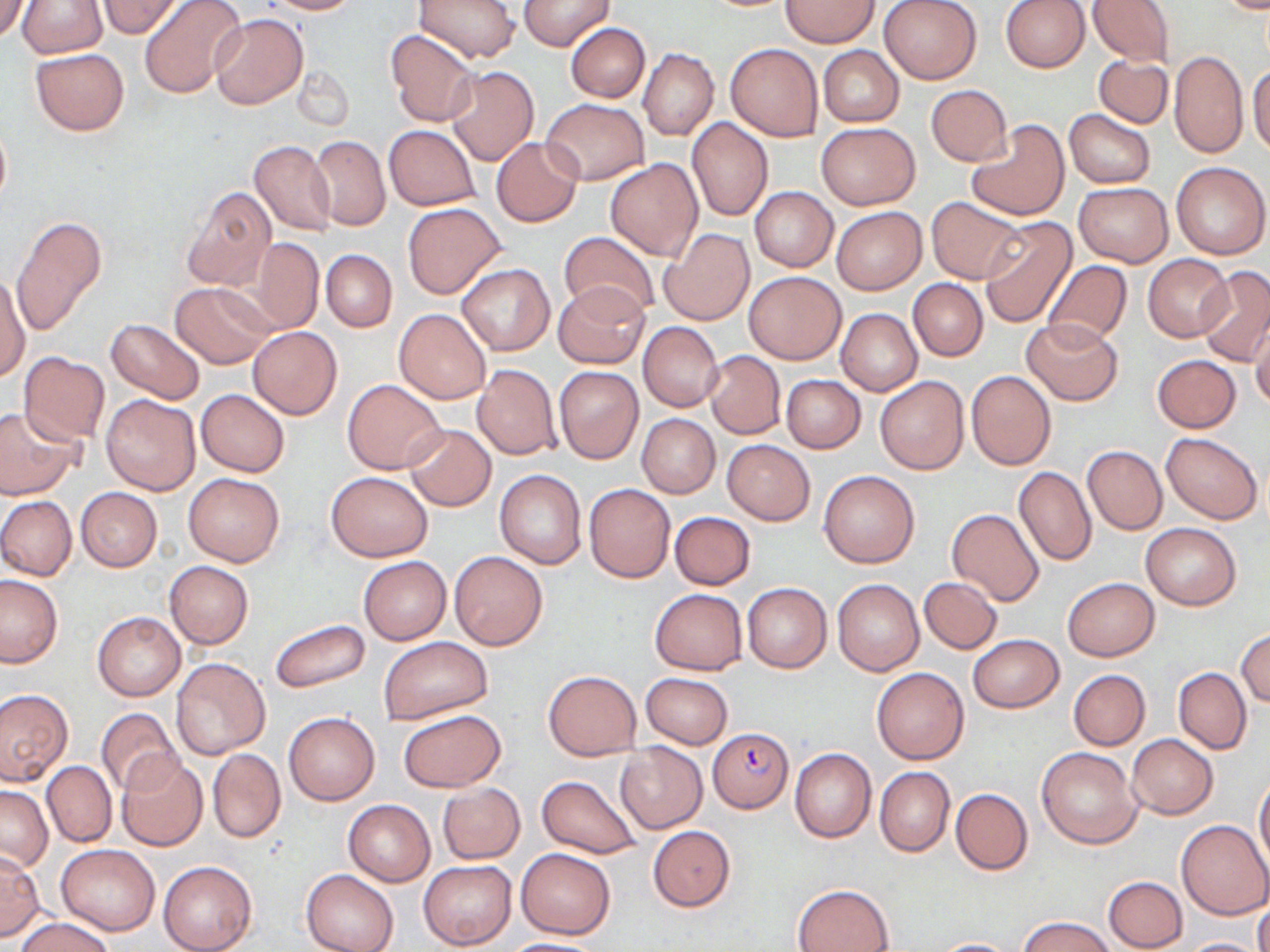
slide-level diagnosis = Plasmodium falciparum
uninfected red blood cell locations = approximate bounding boxes as [x1, y1, x2, y2] in pixels: [1, 0, 30, 41], [137, 0, 247, 99], [261, 0, 361, 15], [415, 0, 520, 64], [518, 0, 615, 51], [782, 0, 881, 47], [877, 0, 982, 84], [1000, 0, 1090, 72], [1087, 0, 1175, 66], [17, 1, 107, 58], [99, 1, 181, 37], [210, 13, 308, 110], [565, 22, 649, 102], [385, 29, 479, 127], [725, 43, 822, 141], [817, 45, 904, 127], [30, 48, 129, 136], [638, 49, 718, 140], [1169, 49, 1249, 159], [1092, 54, 1173, 129], [1248, 63, 1270, 157], [293, 66, 354, 131], [446, 66, 539, 166], [926, 85, 1013, 166], [540, 99, 650, 184], [1064, 109, 1155, 188], [0, 118, 11, 209], [687, 118, 774, 221], [816, 121, 919, 210], [966, 121, 1068, 221], [384, 125, 479, 210], [309, 135, 390, 231], [491, 137, 582, 227], [248, 139, 336, 237], [211, 146, 328, 292], [606, 158, 703, 261], [1170, 162, 1269, 259], [1075, 182, 1172, 265], [181, 186, 275, 292], [750, 186, 838, 272], [927, 196, 1028, 285], [402, 204, 506, 298], [832, 206, 927, 294], [10, 214, 106, 339], [977, 216, 1076, 328], [660, 229, 754, 325], [558, 231, 661, 321], [249, 239, 323, 331], [321, 249, 396, 332], [1144, 254, 1233, 341], [1042, 259, 1133, 347], [456, 264, 554, 356], [1196, 267, 1270, 367], [745, 272, 844, 364], [0, 275, 29, 382], [909, 280, 988, 360], [170, 283, 275, 370], [552, 283, 651, 369], [394, 308, 492, 404], [835, 308, 922, 397], [1249, 317, 1270, 411], [107, 318, 205, 405], [1021, 319, 1123, 405], [638, 322, 722, 412], [248, 326, 342, 419], [703, 350, 786, 439], [20, 353, 109, 443], [1152, 355, 1241, 432], [472, 365, 561, 459], [554, 366, 644, 463], [965, 370, 1057, 471], [782, 375, 865, 452], [875, 375, 969, 474], [343, 379, 446, 474], [196, 390, 289, 477], [102, 394, 201, 497], [0, 406, 80, 498], [637, 413, 721, 498], [404, 424, 496, 510], [1162, 432, 1262, 524], [721, 439, 815, 525], [1082, 446, 1167, 534], [1013, 466, 1096, 566], [818, 469, 919, 568], [495, 470, 587, 569], [183, 471, 284, 566], [326, 471, 433, 561], [584, 483, 675, 582], [77, 487, 162, 571], [0, 496, 76, 581], [946, 508, 1044, 608], [669, 512, 755, 589], [1140, 523, 1243, 609], [449, 552, 548, 650], [358, 555, 452, 644], [164, 560, 253, 649], [0, 575, 62, 667], [919, 576, 1001, 654], [1063, 577, 1158, 660], [832, 579, 924, 676], [741, 583, 832, 673], [649, 588, 747, 675], [93, 612, 185, 700], [270, 618, 371, 693], [1236, 628, 1270, 708], [967, 634, 1063, 712], [380, 637, 493, 722], [170, 657, 271, 760], [872, 667, 969, 764], [1174, 667, 1251, 754], [543, 670, 641, 760], [1069, 670, 1150, 749], [641, 673, 733, 748], [0, 688, 72, 784], [96, 707, 182, 797], [397, 710, 506, 793], [284, 712, 379, 804], [1127, 734, 1217, 818], [614, 742, 708, 833], [1037, 747, 1139, 850], [789, 748, 876, 844], [208, 749, 285, 843], [116, 756, 208, 851], [42, 761, 116, 848], [875, 767, 955, 857], [537, 776, 642, 859], [1254, 776, 1270, 875], [438, 783, 524, 864], [1, 785, 53, 872], [950, 787, 1033, 874], [342, 800, 435, 887], [1177, 818, 1270, 919], [648, 825, 735, 912], [58, 844, 160, 934], [515, 847, 616, 939], [0, 850, 44, 941], [419, 859, 517, 950], [158, 860, 256, 952], [303, 870, 399, 952], [1104, 876, 1188, 951], [793, 884, 895, 951], [1253, 899, 1270, 952], [14, 915, 116, 952], [1019, 916, 1117, 952], [1181, 937, 1265, 952], [499, 938, 608, 951], [929, 938, 1024, 951]
modality = light microscopy
image size = 1270×952 pixels
stain = May-Grünwald-Giemsa
preparation = thin blood film
field of view = single
magnification = 1000x
Plasmodium falciparum-infected red blood cell locations = approximate bounding boxes as [x1, y1, x2, y2] in pixels: [709, 728, 793, 812]